State the preparation type.
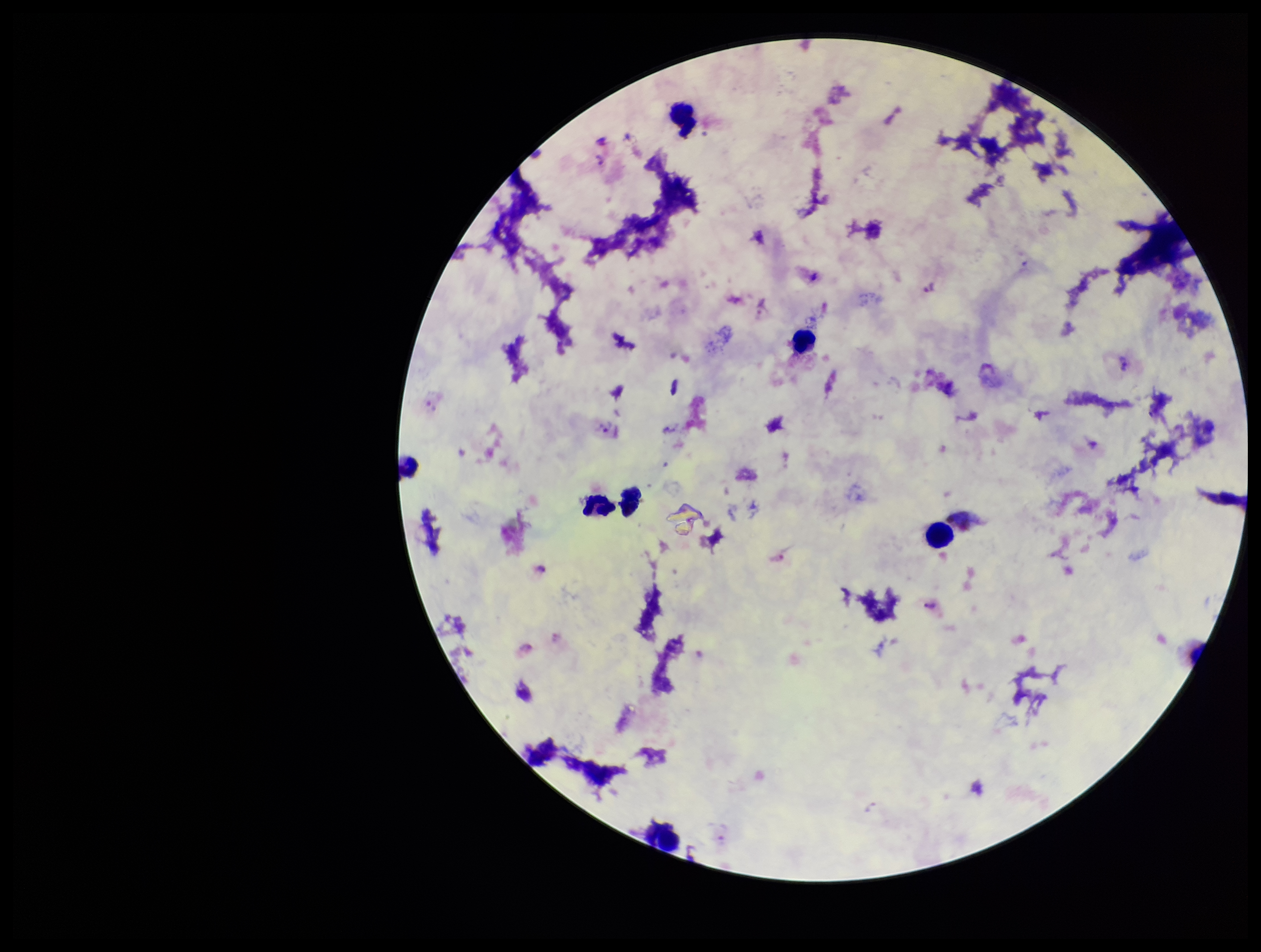
A thick smear.

Plasmodium parasites = detected
image size = 1261×952 pixels
capture = smartphone photograph through the microscope eyepiece
field of view = one from this slide
parasite count = 7
stain = Giemsa
species reported for this patient = Plasmodium vivax
patient malaria status = infected
leukocyte count = 7